Mark where leukocytes are.
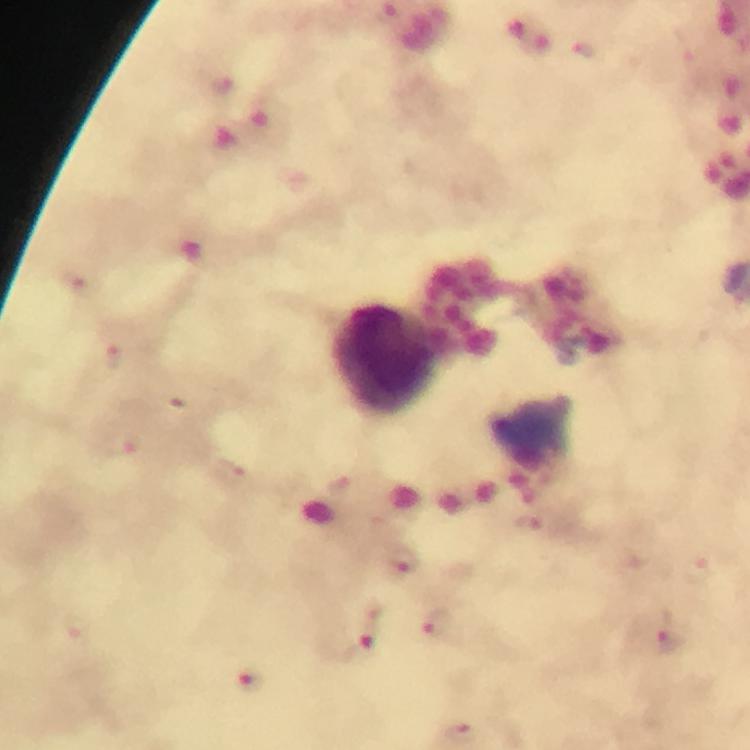

Approximate object centers, in pixels from the top-left corner.
Leukocytes: (x=386, y=360).

Summary:
  - Malaria parasite locations: (x=72, y=285), (x=114, y=358), (x=177, y=407), (x=127, y=449), (x=236, y=475), (x=399, y=558), (x=438, y=623), (x=668, y=636), (x=364, y=637), (x=249, y=680), (x=461, y=732)
  - Image size: 750×750 pixels
  - Stain: Giemsa
  - Immersion oil: applied
  - Magnification: 100x
  - Preparation: thick blood smear
  - Context: from a malaria diagnostic workup
  - Capture: smartphone mounted on the microscope
  - Cropped from: one field of view